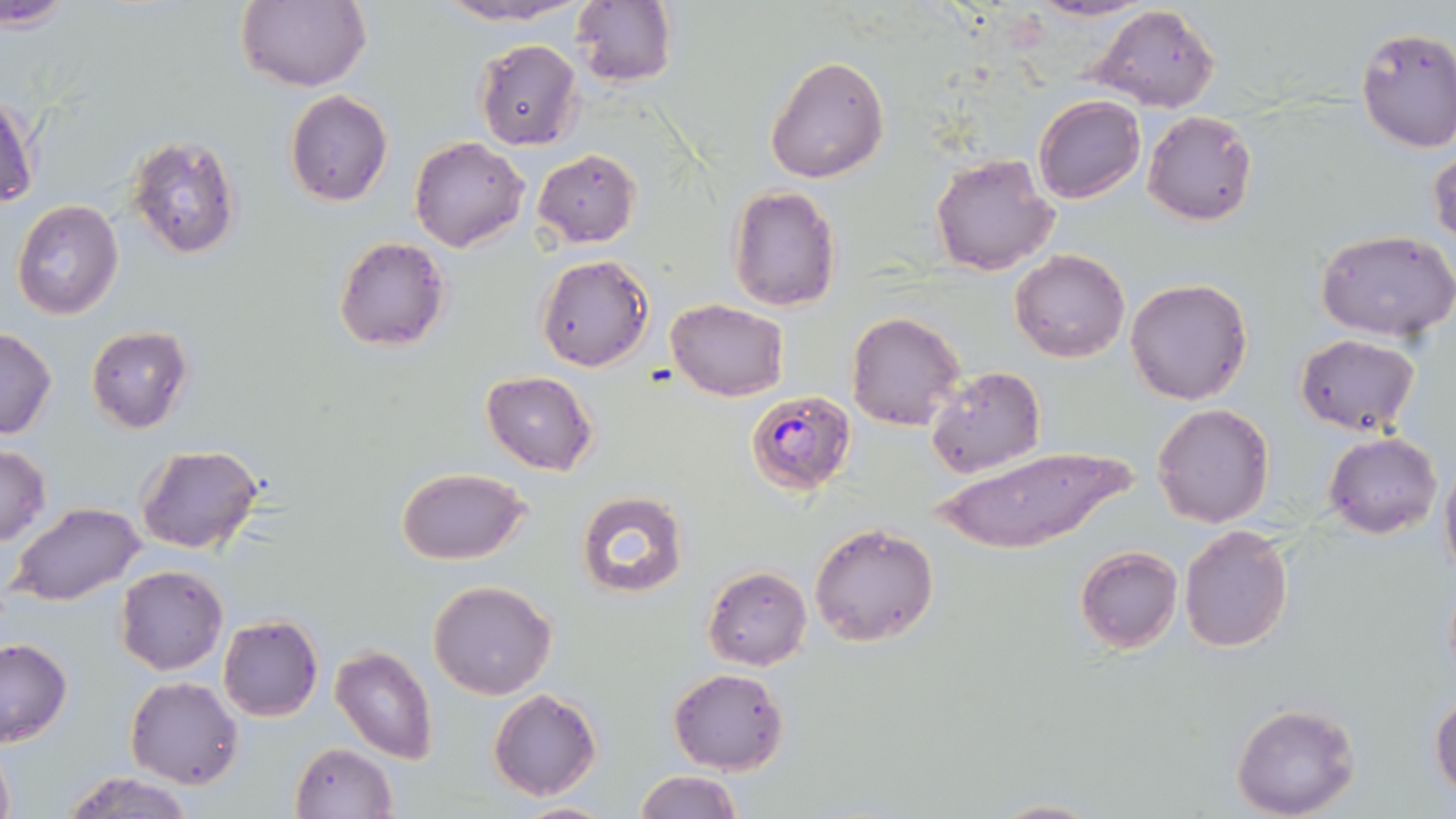

Approximate bounding boxes as (x1, y1, x2, y2) in pixels. Uninfected red blood cell locations: (2, 0, 74, 34), (234, 0, 370, 91), (434, 0, 590, 25), (571, 0, 678, 89), (1024, 0, 1153, 22), (1091, 4, 1221, 113), (1354, 26, 1456, 154), (474, 38, 584, 152), (765, 54, 890, 183), (284, 90, 393, 206), (1, 93, 41, 212), (1032, 95, 1144, 204), (1142, 109, 1257, 228), (125, 132, 244, 261), (409, 137, 529, 253), (1429, 146, 1455, 251), (533, 148, 641, 248), (929, 153, 1058, 276), (725, 185, 843, 313), (10, 199, 124, 321), (1314, 229, 1456, 342), (333, 238, 450, 351), (1009, 248, 1129, 363), (535, 253, 654, 372), (1124, 278, 1253, 405), (665, 299, 789, 402), (846, 309, 966, 431), (85, 326, 193, 433), (0, 328, 56, 439), (1295, 333, 1420, 437), (924, 365, 1046, 480), (481, 370, 598, 475), (1152, 403, 1275, 530), (1324, 431, 1442, 539), (136, 443, 265, 555), (0, 445, 50, 544), (936, 445, 1142, 554), (1439, 452, 1456, 586), (395, 467, 531, 564), (574, 491, 690, 600), (9, 502, 145, 607), (809, 521, 940, 648), (1180, 524, 1293, 653), (1074, 545, 1182, 655), (114, 564, 229, 676), (702, 565, 814, 671), (428, 579, 557, 700), (218, 615, 323, 722), (0, 638, 73, 746), (330, 645, 437, 763), (667, 667, 788, 775), (126, 677, 243, 789), (488, 688, 603, 801), (1429, 689, 1455, 801), (1229, 702, 1361, 819), (0, 742, 14, 819), (291, 742, 397, 819), (60, 770, 198, 819), (634, 771, 743, 819), (988, 798, 1102, 819), (504, 801, 621, 819). Plasmodium falciparum-infected red blood cell locations: (745, 390, 856, 495). Slide-level diagnosis: Plasmodium falciparum. 1000x magnification. Thin blood film. Image is 1456×819 pixels. Optical microscopy. Single field of view. May-Grünwald-Giemsa-stained preparation.